Describe the morphology of the red blood cells.
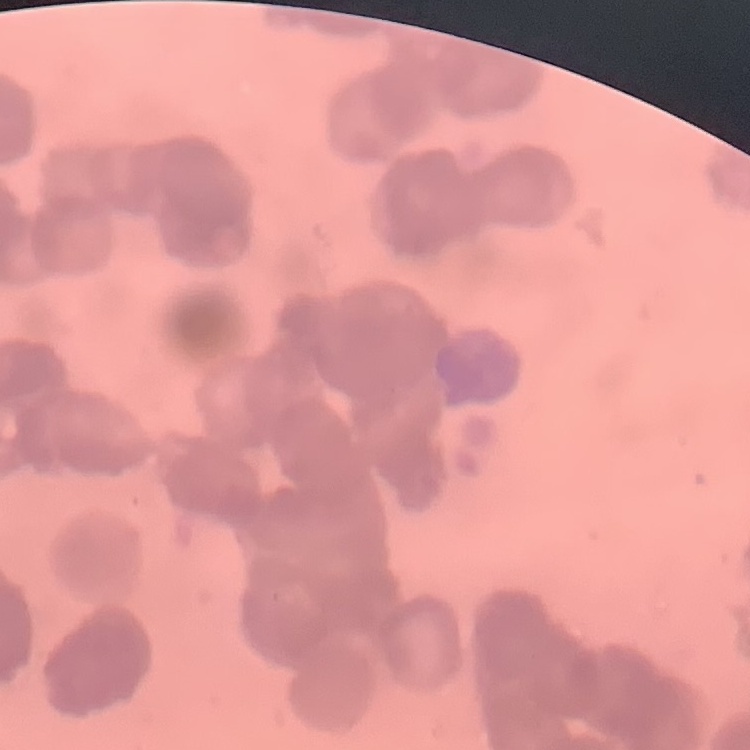
They show rouleaux formation.

Field's or Giemsa stain. One tile cut from a larger photomicrograph. Thin blood film.